Assess the morphology of the red blood cells.
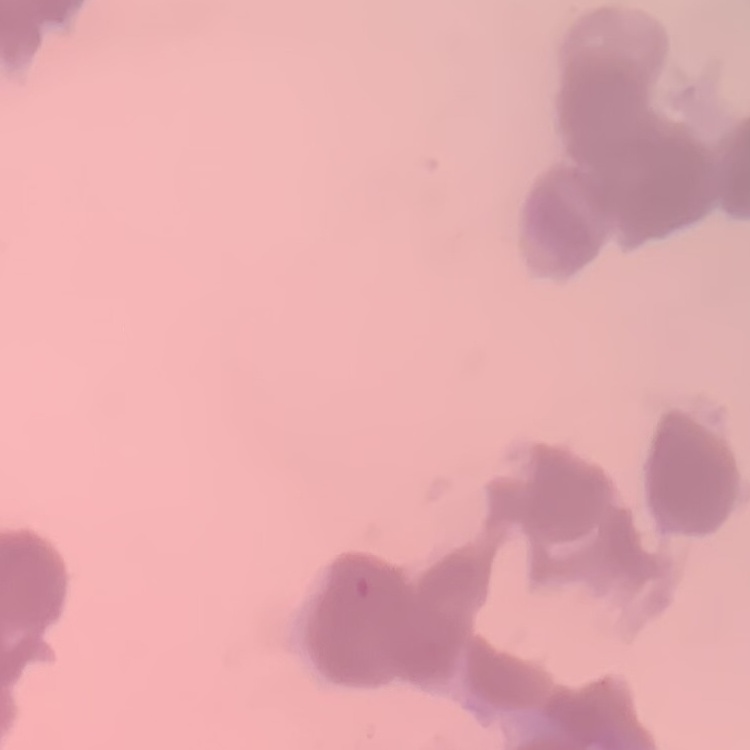

Rouleaux formation.

image_type: one tile cut from a larger photomicrograph
preparation: thin blood smear
stain: Field's or Giemsa